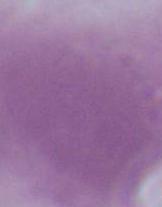

modality = micrograph
identification = red blood cell
magnification = 1000x